Name the blood parasite species.
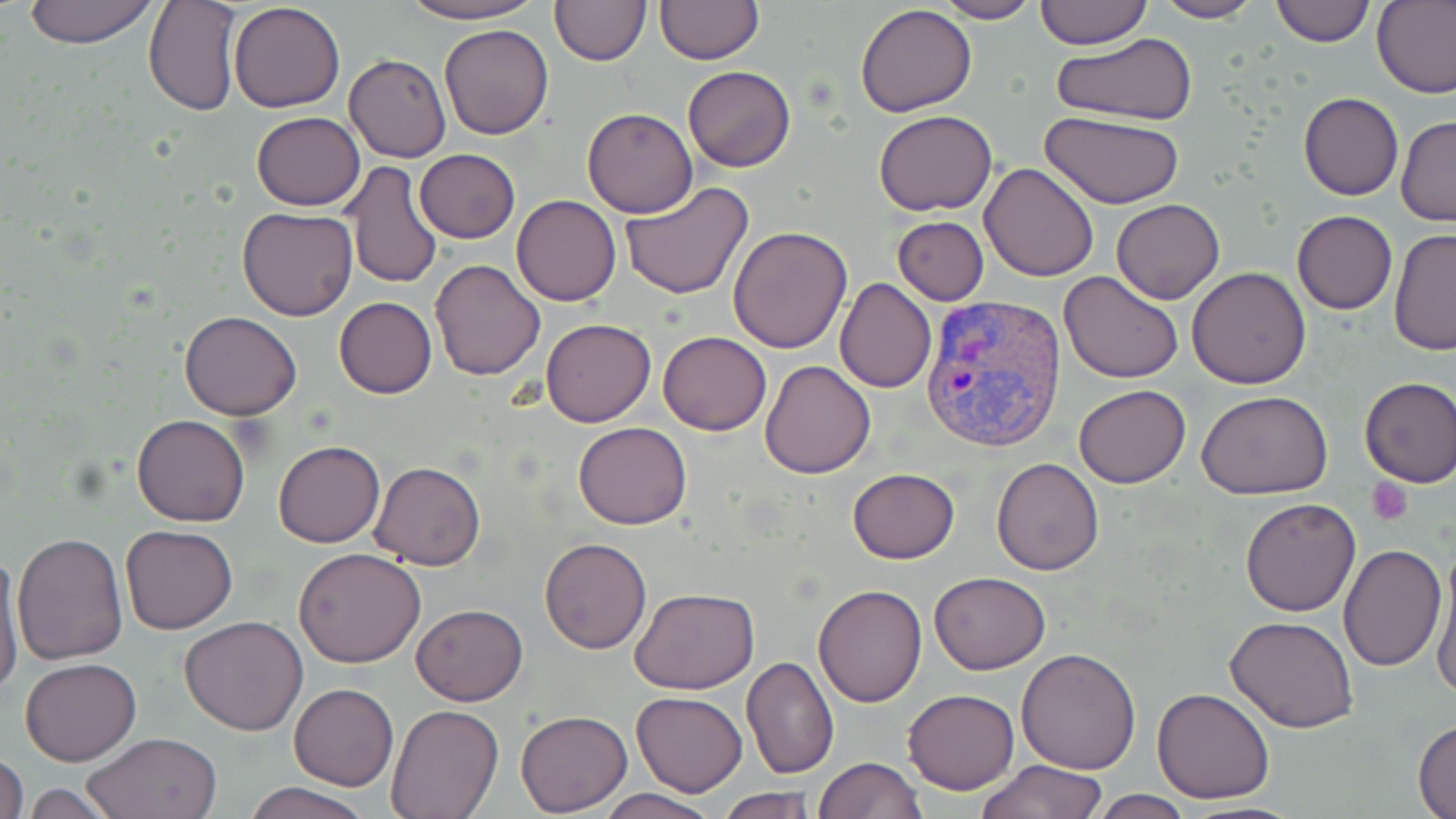

Plasmodium vivax.

Approximate bounding boxes as (x1,y1)-(x2,y2) corner pairs in pixels. Plasmodium vivax-infected red blood cell locations: (919,289)-(1066,455). Uninfected red blood cell locations: (22,0)-(162,48), (143,0)-(242,118), (392,0)-(544,24), (549,0)-(649,66), (655,0)-(762,64), (931,0)-(1039,23), (1033,0)-(1151,48), (1151,0)-(1262,23), (1269,0)-(1375,47), (1374,1)-(1456,99), (228,2)-(346,114), (855,4)-(977,116), (439,24)-(554,142), (1050,31)-(1199,126), (343,54)-(451,163), (682,65)-(796,173), (1298,92)-(1403,201), (582,107)-(699,218), (873,109)-(997,216), (251,111)-(365,210), (1040,111)-(1185,208), (1397,115)-(1456,227), (414,148)-(520,243), (979,161)-(1101,282), (341,162)-(441,289), (621,181)-(753,300), (512,194)-(621,306), (1112,198)-(1224,304), (237,208)-(358,320), (1293,211)-(1397,314), (893,217)-(988,304), (728,226)-(853,354), (1389,228)-(1456,358), (428,259)-(546,381), (1186,267)-(1311,390), (1059,270)-(1184,384), (834,277)-(936,393), (334,296)-(437,398), (179,311)-(303,420), (541,319)-(655,426), (658,331)-(771,435), (759,359)-(876,478), (1357,376)-(1455,488), (1074,385)-(1191,489), (1196,390)-(1334,498), (132,414)-(250,526), (574,421)-(691,529), (275,441)-(384,548), (991,456)-(1104,575), (370,460)-(485,570), (847,467)-(960,563), (1241,497)-(1361,617), (119,524)-(238,634), (11,531)-(127,665), (539,538)-(652,655), (1339,543)-(1446,669), (1,546)-(25,696), (293,547)-(425,667), (1430,550)-(1456,702), (928,572)-(1051,674), (811,583)-(926,706), (631,588)-(760,694), (410,604)-(526,705), (179,616)-(310,736), (1227,616)-(1358,732), (1016,648)-(1142,773), (741,654)-(839,778), (20,657)-(141,767), (289,683)-(398,790), (1152,686)-(1275,803), (903,687)-(1020,795), (631,690)-(748,796), (387,703)-(505,818), (515,709)-(632,816), (1413,717)-(1456,819), (82,731)-(222,819), (0,751)-(28,819), (815,757)-(925,818), (976,759)-(1108,819), (243,781)-(375,819), (22,782)-(122,816), (596,788)-(721,819), (716,788)-(819,819), (1086,790)-(1194,818). Platelet locations: (1367,476)-(1414,525). Light microscopy. Image is 1456×819 pixels. May-Grünwald-Giemsa stain. 1000x magnification. One field of a larger specimen. Thin blood film.